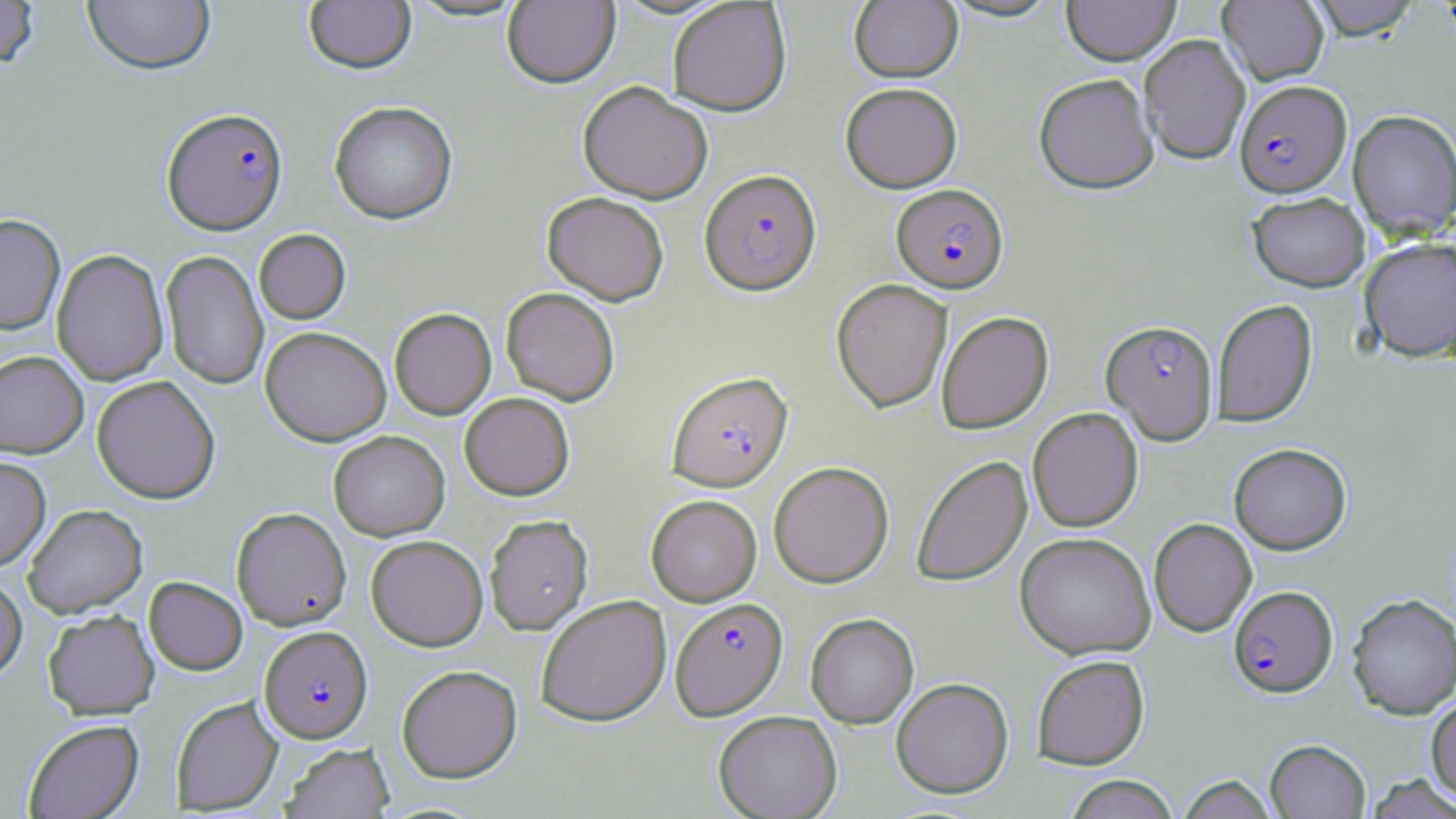

{
  "plasmodium_falciparum_infected_red_blood_cell_locations": "approximate bounding boxes as (x1, y1, x2, y2) in pixels: (1234, 80, 1352, 197), (162, 107, 288, 234), (699, 169, 821, 295), (891, 184, 1009, 293), (1101, 320, 1218, 444), (667, 371, 792, 491), (1229, 585, 1337, 697), (670, 597, 788, 720), (260, 625, 372, 743)",
  "slide_level_diagnosis": "Plasmodium falciparum",
  "image_size": "1456×819 pixels",
  "magnification": "1000x",
  "modality": "optical microscopy",
  "preparation": "thin blood film",
  "uninfected_red_blood_cell_locations": "approximate bounding boxes as (x1, y1, x2, y2) in pixels: (82, 0, 216, 76), (405, 0, 530, 22), (502, 0, 620, 89), (941, 0, 1063, 23), (1062, 0, 1180, 65), (1218, 0, 1329, 85), (1308, 0, 1421, 40), (0, 1, 39, 70), (303, 1, 416, 75), (667, 1, 791, 116), (849, 1, 963, 83), (1139, 34, 1251, 165), (1033, 73, 1159, 194), (577, 81, 713, 204), (841, 82, 962, 193), (329, 101, 458, 225), (1347, 109, 1456, 240), (542, 192, 669, 305), (1248, 192, 1370, 292), (0, 214, 66, 335), (254, 229, 351, 325), (1358, 237, 1456, 362), (51, 249, 169, 385), (160, 250, 270, 390), (831, 279, 952, 412), (500, 287, 620, 405), (1212, 298, 1317, 428), (389, 307, 496, 420), (936, 311, 1054, 434), (260, 326, 391, 446), (0, 351, 88, 457), (91, 376, 221, 504), (459, 392, 574, 500), (1028, 407, 1143, 532), (329, 431, 450, 540), (1229, 443, 1351, 554), (0, 456, 51, 571), (911, 456, 1032, 588), (769, 461, 894, 588), (645, 494, 762, 605), (23, 505, 147, 618), (231, 508, 351, 630), (484, 514, 593, 635), (1149, 518, 1257, 636), (1014, 532, 1156, 660), (366, 535, 488, 650), (0, 574, 27, 682), (144, 576, 247, 675), (1347, 594, 1456, 720), (535, 595, 671, 726), (43, 609, 159, 720), (805, 613, 919, 728), (1031, 654, 1149, 769), (397, 665, 522, 783), (891, 677, 1013, 798), (1426, 695, 1456, 801), (171, 696, 283, 815), (713, 710, 842, 819), (23, 719, 144, 818), (1265, 739, 1370, 818), (281, 743, 395, 819), (1363, 773, 1456, 818), (1064, 775, 1179, 819), (1177, 775, 1278, 819)",
  "field_of_view": "one of a larger specimen",
  "stain": "May-Grünwald-Giemsa"
}